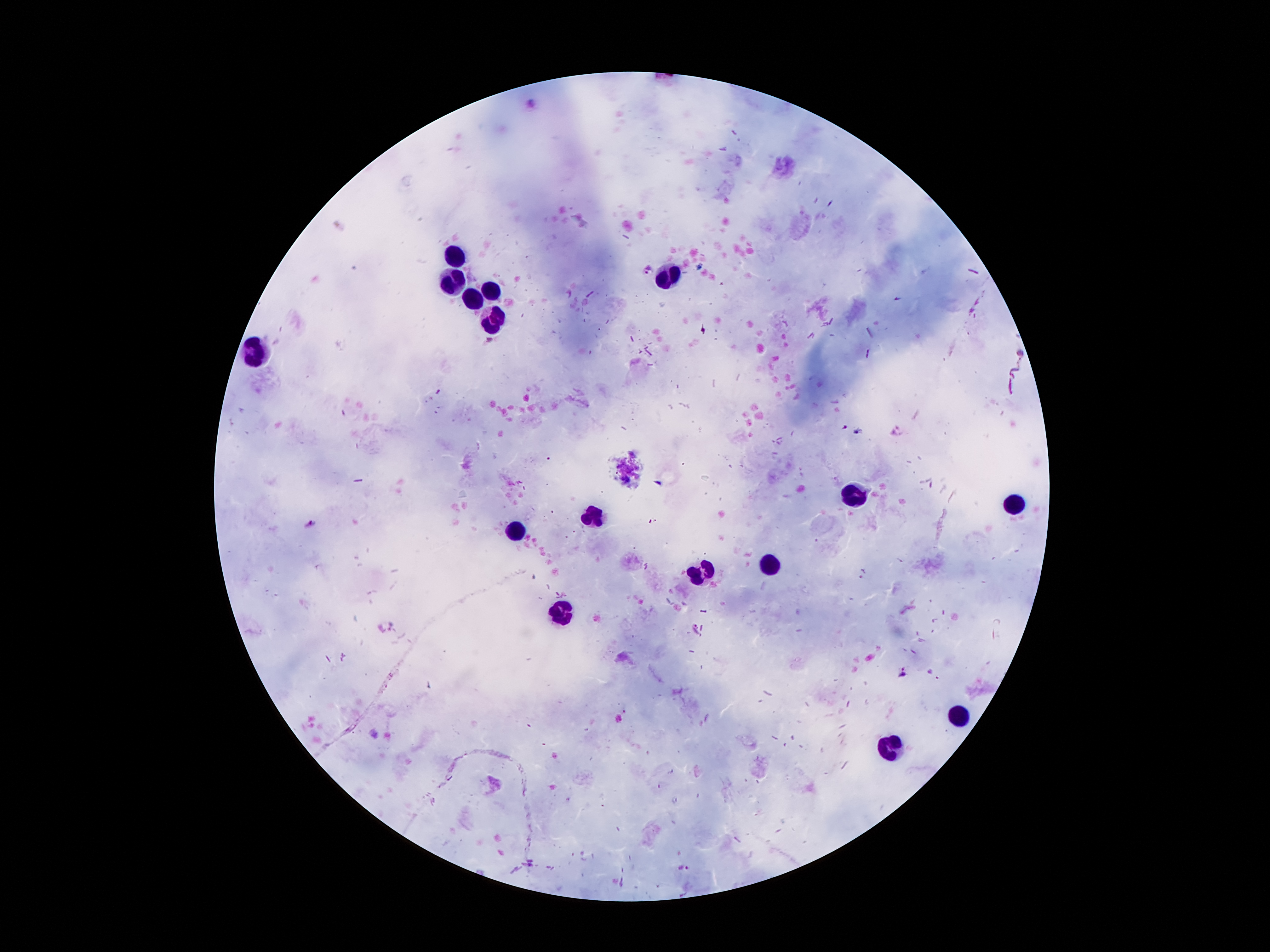
Approximate object centers, in pixels from the top-left corner. Malaria parasite locations: (x=648, y=269), (x=310, y=524), (x=386, y=626), (x=695, y=630), (x=904, y=673), (x=683, y=866). Leukocyte locations: (x=453, y=256), (x=670, y=275), (x=451, y=283), (x=490, y=288), (x=473, y=299), (x=490, y=319), (x=257, y=350), (x=854, y=496), (x=1013, y=503), (x=593, y=513), (x=518, y=528), (x=703, y=564), (x=770, y=566), (x=562, y=614), (x=962, y=713), (x=895, y=748). 100x magnification. Patient malaria status: positive for Plasmodium falciparum. Giemsa-stained preparation. Image is 1270×952 pixels. One field from this slide. Thick peripheral-blood smear. Smartphone photograph taken through the microscope eyepiece.